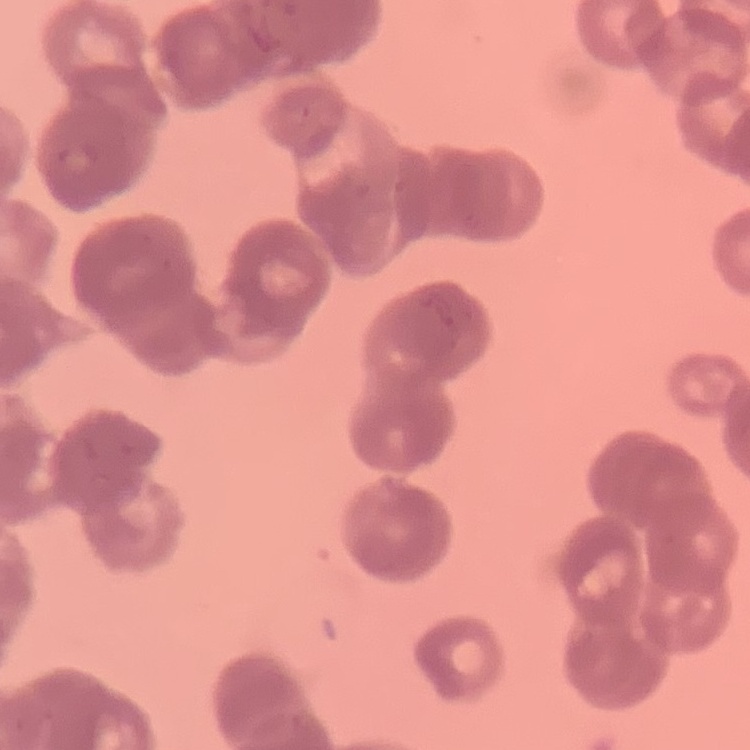

Summary:
  - Erythrocyte morphology: rouleaux formation
  - Preparation: thin peripheral smear
  - Stain: Field's or Giemsa
  - Image type: one tile cut from a larger photomicrograph